Locate every blood parasite and identify its species.
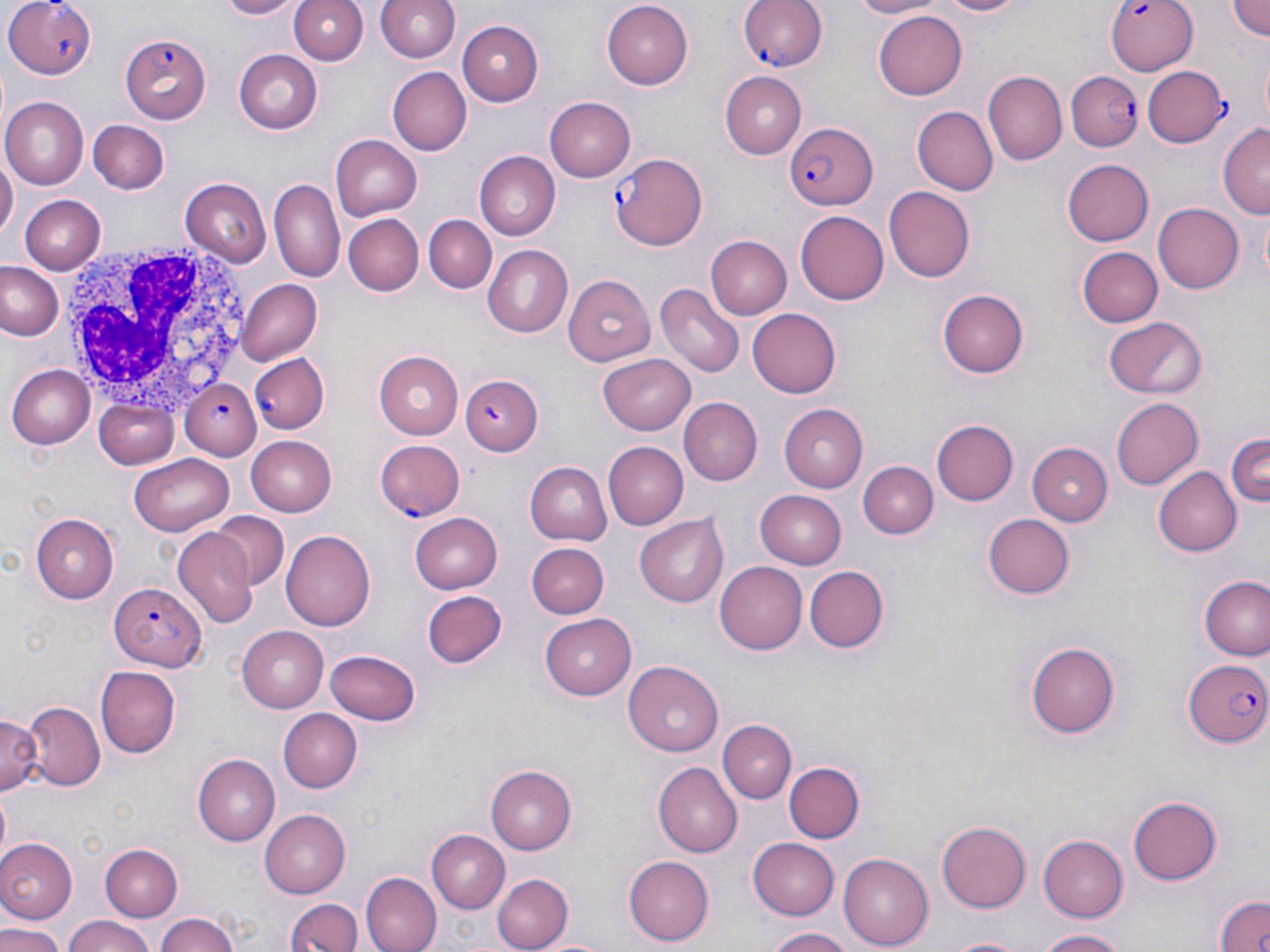

Approximate bounding boxes as [x1, y1, x2, y2] in pixels.
Plasmodium falciparum-infected red blood cells: [4, 0, 97, 80], [737, 0, 828, 73], [1109, 0, 1202, 77], [119, 34, 209, 123], [1142, 67, 1228, 148], [1067, 72, 1145, 150], [786, 121, 879, 209], [609, 152, 708, 250], [249, 354, 329, 433], [459, 375, 543, 455], [179, 379, 261, 459], [108, 579, 209, 673], [1182, 658, 1270, 748].
No Plasmodium ovale, Plasmodium malariae, Plasmodium vivax, Babesia divergens, or Trypanosoma brucei observed.

Summary:
  - White blood cell locations: [55, 237, 252, 416]
  - Uninfected red blood cell locations: [213, 0, 305, 19], [290, 0, 367, 66], [375, 0, 462, 62], [845, 0, 946, 19], [923, 0, 1031, 18], [1226, 0, 1270, 42], [601, 2, 692, 89], [872, 8, 966, 100], [456, 19, 543, 104], [234, 50, 323, 135], [387, 68, 470, 155], [719, 72, 806, 158], [982, 72, 1066, 167], [2, 96, 88, 188], [545, 97, 636, 180], [916, 106, 998, 195], [87, 117, 171, 195], [1218, 123, 1270, 217], [330, 135, 423, 221], [475, 151, 560, 238], [0, 157, 14, 246], [1061, 160, 1154, 245], [180, 178, 271, 266], [270, 179, 345, 285], [883, 186, 975, 283], [18, 194, 105, 273], [1152, 203, 1243, 295], [796, 212, 889, 304], [1256, 212, 1270, 287], [345, 213, 424, 296], [424, 216, 496, 293], [707, 228, 875, 313], [708, 235, 792, 321], [483, 246, 573, 338], [1076, 246, 1161, 328], [0, 262, 65, 342], [562, 273, 656, 366], [234, 279, 321, 366], [657, 283, 743, 377], [938, 290, 1029, 377], [748, 307, 844, 397], [1104, 315, 1206, 400], [373, 351, 464, 439], [598, 355, 694, 435], [8, 363, 93, 448], [679, 397, 763, 483], [1112, 397, 1205, 490], [95, 398, 179, 468], [776, 402, 866, 494], [931, 419, 1018, 505], [1224, 431, 1269, 513], [246, 435, 336, 516], [376, 439, 465, 521], [602, 442, 687, 529], [1028, 443, 1113, 525], [132, 452, 234, 532], [857, 460, 937, 538], [525, 461, 611, 546], [1153, 467, 1243, 557], [756, 489, 846, 567], [211, 511, 289, 590], [408, 513, 501, 593], [637, 513, 731, 607], [30, 514, 119, 603], [982, 514, 1075, 598], [280, 528, 375, 633], [172, 529, 257, 627], [528, 543, 606, 619], [715, 560, 811, 654], [805, 567, 890, 652], [1197, 574, 1270, 661], [422, 591, 508, 669], [542, 611, 640, 699], [237, 625, 329, 712], [1026, 640, 1120, 736], [326, 647, 422, 725], [624, 661, 723, 758], [94, 665, 179, 758], [22, 700, 104, 788], [280, 708, 363, 791], [0, 714, 45, 801], [717, 720, 795, 804], [194, 752, 281, 845], [782, 761, 863, 844], [654, 763, 742, 856], [486, 764, 577, 853], [0, 792, 12, 857], [1128, 795, 1223, 884], [260, 808, 352, 898], [937, 820, 1033, 913], [427, 829, 509, 911], [1039, 834, 1128, 922], [749, 835, 843, 919], [0, 837, 78, 921], [98, 844, 182, 922], [837, 852, 933, 951], [624, 855, 714, 944], [362, 871, 442, 952], [493, 872, 571, 951], [1214, 893, 1270, 952], [284, 896, 364, 952], [152, 912, 243, 952], [59, 915, 156, 952], [0, 924, 65, 952], [765, 926, 853, 952], [1037, 928, 1131, 951], [943, 934, 1030, 952]
  - Slide-level diagnosis: Plasmodium falciparum
  - Modality: optical microscopy
  - Stain: May-Grünwald-Giemsa
  - Preparation: thin blood smear
  - Magnification: 1000x
  - Field of view: single
  - Image size: 1270×952 pixels